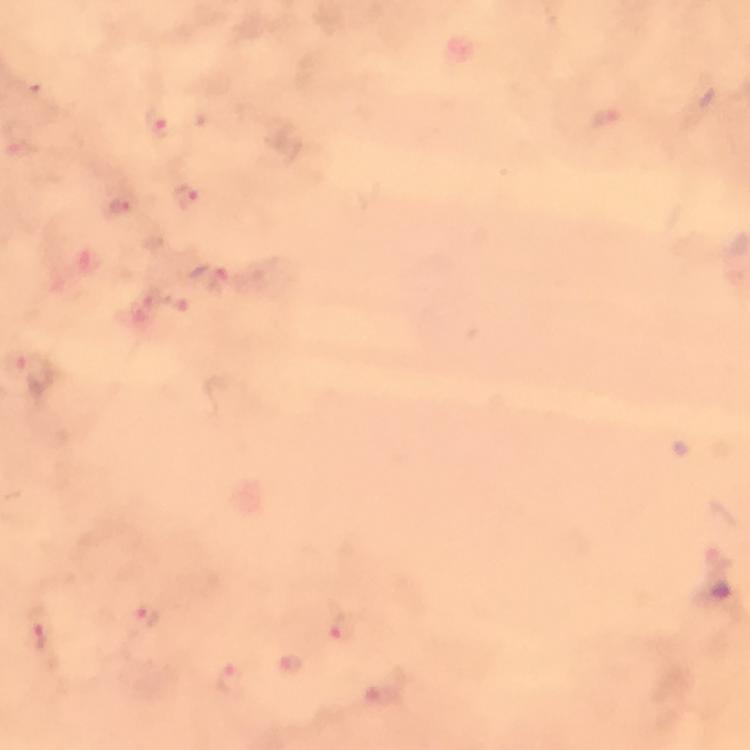

Approximate object centers, in pixels from the top-left corner.
Summary:
  - Plasmodium parasite locations: (x=160, y=120), (x=188, y=197), (x=123, y=204), (x=211, y=279), (x=149, y=615), (x=39, y=628), (x=339, y=634), (x=291, y=665), (x=230, y=681)
  - Context: from a malaria diagnostic workup
  - Stain: Giemsa
  - Image size: 750×750 pixels
  - Cropped from: one field of view
  - Capture: smartphone camera through the microscope
  - Immersion oil: used
  - Magnification: 100x
  - Preparation: thick smear